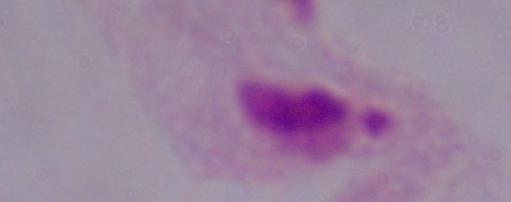
{
  "magnification": "1000x",
  "identification": "trichomonad",
  "modality": "micrograph"
}